Assess this cell for malaria.
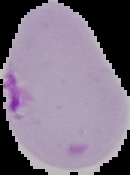

Parasitized.

preparation = thin blood smear
image type = segmented cell region with the area outside set to black
image size = 130×175 pixels